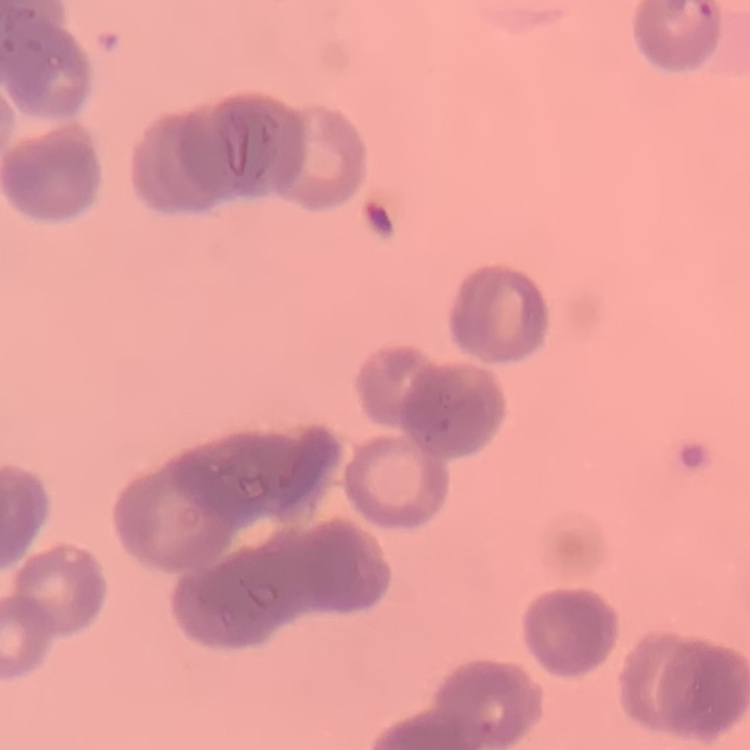
The red blood cells exhibit rouleaux formation. Stained with either Field's or Giemsa. Thin peripheral smear. Square crop of a larger photomicrograph.